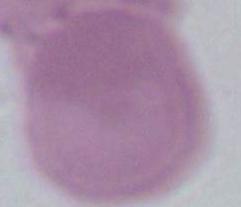
{
  "modality": "micrograph",
  "magnification": "1000x",
  "identification": "red blood cell"
}